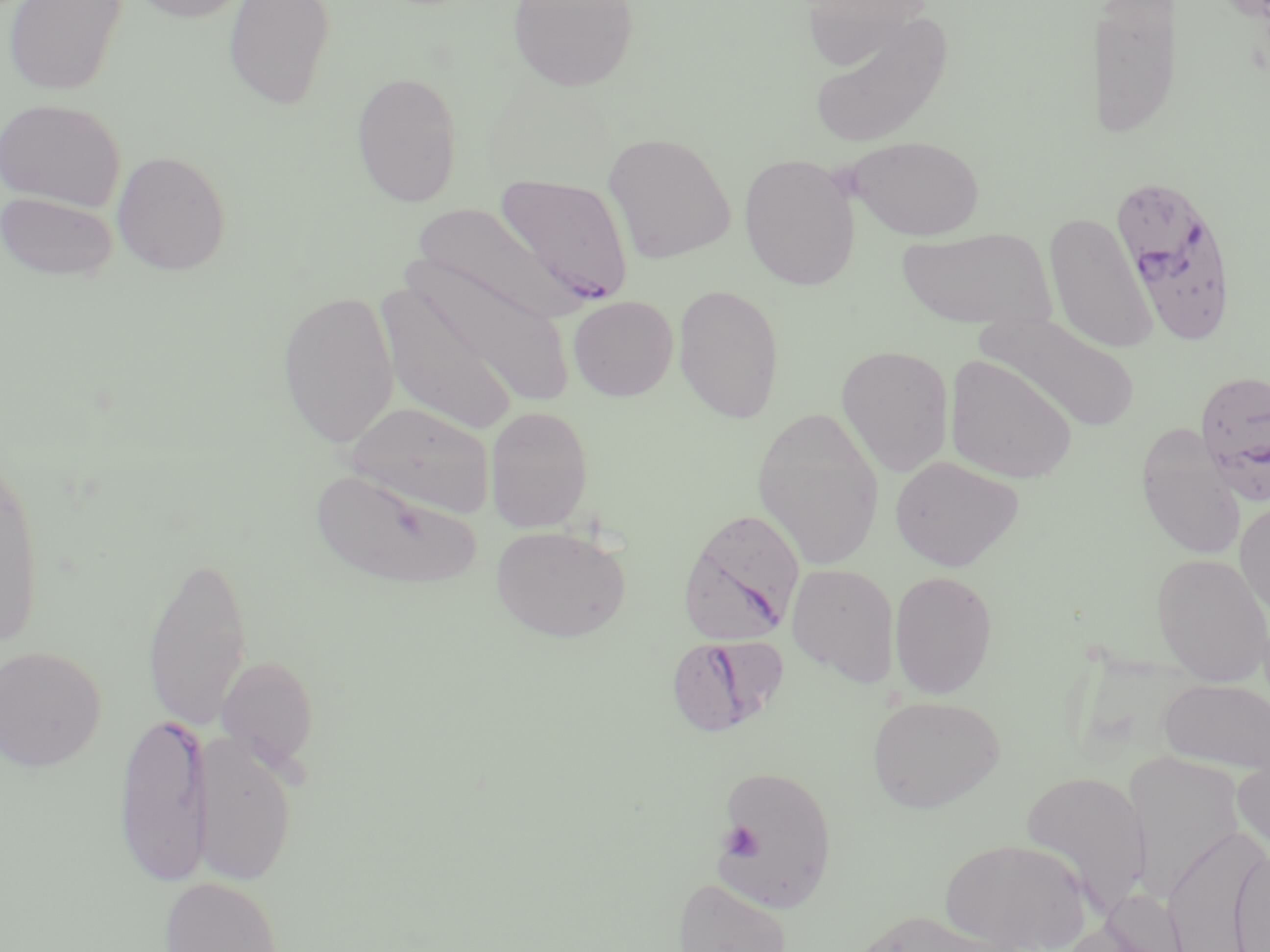 Approximate bounding boxes as (x1,y1)-(x2,y2) corner pairs in pixels. Plasmodium falciparum-infected red blood cell locations: (494,172)-(635,308), (1111,175)-(1241,346), (1194,368)-(1270,503), (677,508)-(805,646), (665,634)-(782,737), (112,712)-(213,887). Platelet locations: (721,821)-(762,860). Uninfected red blood cell locations: (3,0)-(128,96), (124,0)-(255,22), (223,0)-(336,110), (507,0)-(640,92), (798,0)-(933,69), (1090,1)-(1181,144), (806,11)-(954,149), (350,71)-(463,208), (0,98)-(126,211), (603,132)-(736,264), (846,135)-(985,241), (111,150)-(231,275), (739,153)-(861,290), (1,191)-(118,282), (410,202)-(572,322), (1043,212)-(1158,355), (896,226)-(1054,330), (407,254)-(577,411), (376,280)-(521,436), (673,283)-(785,424), (277,289)-(399,450), (568,295)-(678,401), (976,310)-(1141,433), (836,345)-(955,477), (944,353)-(1078,484), (345,401)-(496,518), (484,406)-(594,533), (751,406)-(886,570), (1137,433)-(1247,561), (0,450)-(47,653), (890,455)-(1024,572), (309,469)-(480,591), (1235,498)-(1270,623), (491,525)-(632,643), (141,547)-(253,741), (1151,553)-(1270,685), (787,563)-(900,685), (889,570)-(998,699), (0,645)-(107,773), (216,653)-(319,772), (1158,678)-(1270,772), (867,694)-(1005,813), (192,732)-(299,886), (1233,748)-(1270,862), (1123,754)-(1246,899), (715,763)-(838,912), (1019,770)-(1153,916), (1163,828)-(1268,952), (939,837)-(1092,951), (1230,848)-(1270,952), (158,876)-(283,952), (673,877)-(791,952), (1092,888)-(1191,951), (842,910)-(1022,952). Slide-level diagnosis: Plasmodium falciparum. Image is 1270×952 pixels. One field of a larger specimen. Thin blood smear. Optical microscopy. May-Grünwald-Giemsa stain. Captured at 1000x magnification.